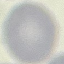 Malaria status: uninfected. Automatically extracted cell patch, resized to 64 × 64 pixels. Giemsa-stained preparation. Photographed with a smartphone camera at the microscope eyepiece. Thin smear of blood.